Locate and identify every blood parasite.
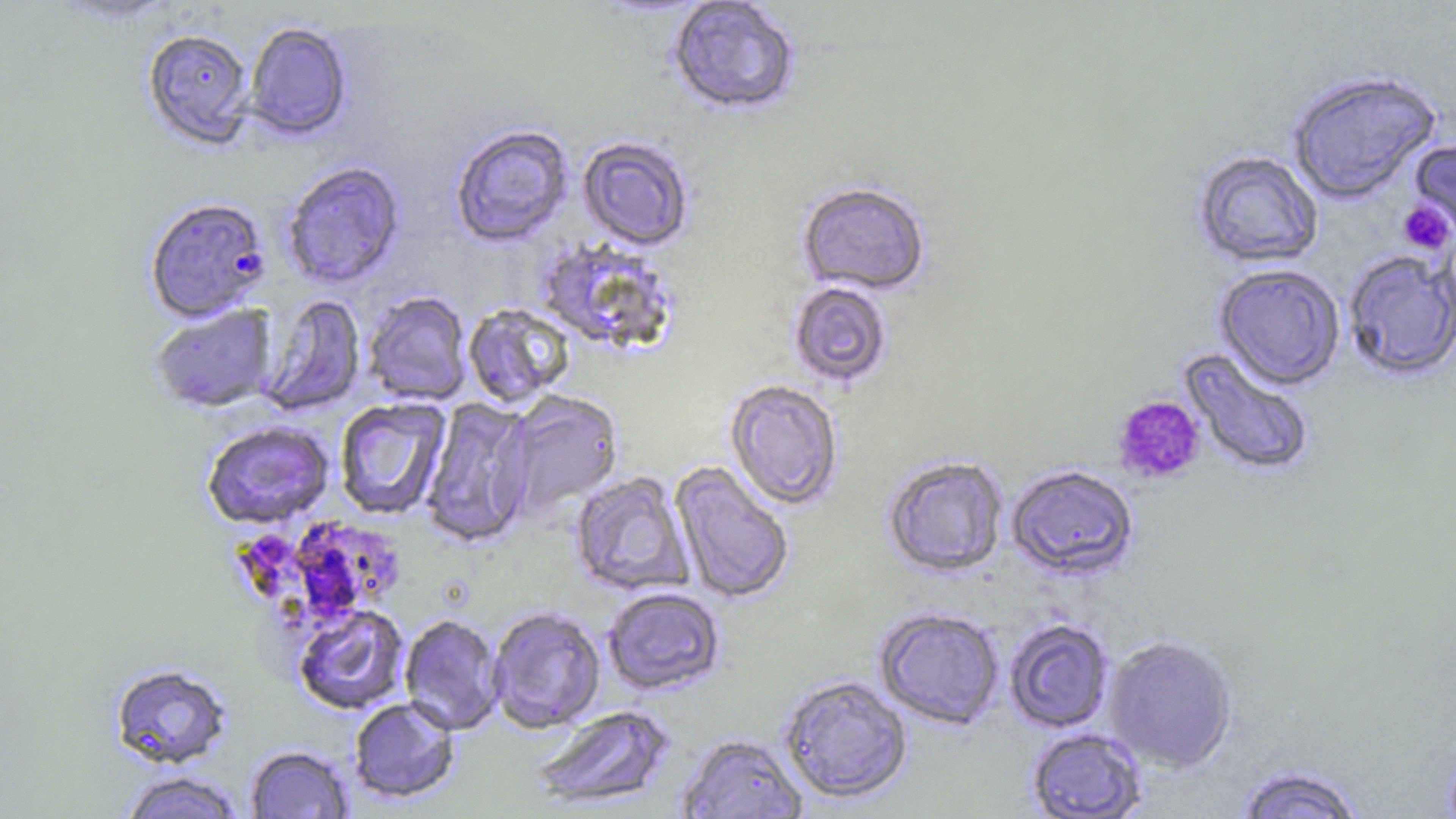
Approximate bounding boxes as (x1,y1)-(x2,y2) corner pairs in pixels.
Plasmodium falciparum-infected red blood cells: (144,197)-(271,323).
No Plasmodium ovale, Plasmodium malariae, Plasmodium vivax, Babesia divergens, or Trypanosoma brucei observed.

{
  "slide_level_diagnosis": "Plasmodium falciparum",
  "image_size": "1456×819 pixels",
  "preparation": "thin blood smear",
  "platelet_locations": "approximate bounding boxes as (x1,y1)-(x2,y2) corner pairs in pixels: (1397,200)-(1454,254), (1113,395)-(1205,485)",
  "magnification": "1000x",
  "modality": "light microscopy",
  "uninfected_red_blood_cell_locations": "approximate bounding boxes as (x1,y1)-(x2,y2) corner pairs in pixels: (666,1)-(801,117), (243,21)-(353,141), (142,29)-(256,151), (1286,69)-(1443,204), (449,124)-(573,247), (1409,135)-(1456,248), (577,136)-(695,251), (1193,149)-(1324,268), (281,162)-(406,290), (797,181)-(931,295), (536,239)-(679,355), (1342,249)-(1456,381), (1213,263)-(1346,389), (787,280)-(893,388), (362,292)-(473,406), (257,294)-(366,417), (462,303)-(575,407), (150,304)-(278,413), (1178,346)-(1317,478), (724,379)-(844,510), (504,391)-(623,516), (334,397)-(451,521), (420,397)-(536,549), (201,421)-(334,529), (881,455)-(1008,577), (669,461)-(795,605), (1006,464)-(1140,581), (570,471)-(694,596), (602,587)-(726,695), (293,604)-(410,715), (487,606)-(606,734), (874,607)-(1005,729), (399,613)-(505,735), (1004,618)-(1115,733), (1102,634)-(1238,773), (109,663)-(233,769), (778,674)-(913,804), (348,696)-(461,803), (531,704)-(674,810), (1026,727)-(1148,818), (675,733)-(808,818), (245,744)-(354,818), (1232,764)-(1369,818), (116,770)-(246,819)",
  "stain": "May-Grünwald-Giemsa",
  "field_of_view": "one of a larger specimen"
}